Assess this cell for malaria.
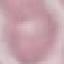

It is uninfected.

{
  "capture": "smartphone camera at the microscope eyepiece",
  "stain": "Giemsa",
  "preparation": "thin blood film",
  "image_type": "cell patch, automatically extracted from a larger field of view and resized to 64 × 64 pixels"
}